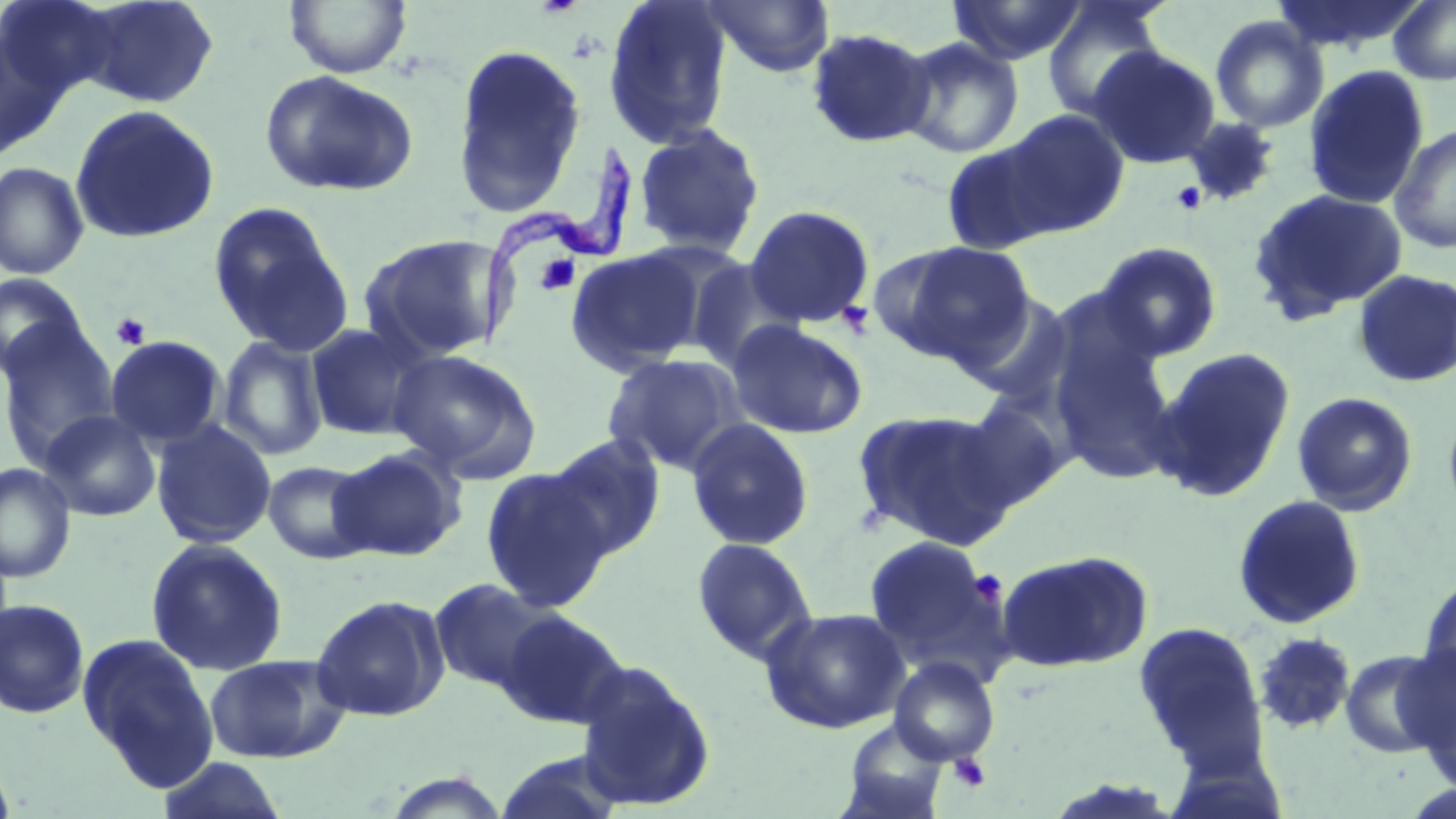
Summary:
  - Coordinate format: approximate bounding boxes as (x1, y1, x2, y2) in pixels
  - Platelet locations: (1172, 182, 1206, 214), (535, 254, 581, 296), (844, 301, 878, 333), (110, 313, 151, 349), (967, 569, 1008, 606), (947, 753, 991, 793)
  - Uninfected red blood cell locations: (1, 0, 115, 107), (75, 0, 220, 108), (284, 0, 411, 78), (602, 0, 734, 150), (701, 0, 835, 78), (947, 0, 1088, 66), (1388, 0, 1456, 86), (1041, 1, 1169, 122), (1210, 15, 1328, 132), (805, 27, 936, 149), (0, 31, 61, 161), (897, 37, 1025, 159), (450, 42, 588, 217), (1088, 45, 1221, 168), (1303, 64, 1430, 210), (259, 69, 418, 198), (68, 104, 220, 244), (999, 108, 1130, 238), (1182, 116, 1281, 206), (1390, 122, 1456, 254), (632, 123, 766, 258), (941, 138, 1061, 255), (0, 161, 90, 280), (1247, 187, 1408, 324), (207, 202, 353, 357), (745, 205, 875, 328), (359, 234, 507, 363), (874, 240, 1036, 366), (1094, 241, 1223, 361), (566, 247, 706, 374), (686, 259, 803, 373), (1352, 269, 1456, 389), (0, 274, 88, 380), (953, 288, 1077, 411), (0, 320, 121, 468), (726, 320, 868, 440), (304, 323, 429, 442), (1048, 327, 1185, 485), (105, 335, 226, 448), (217, 335, 328, 462), (1151, 348, 1296, 502), (387, 350, 542, 479), (601, 354, 747, 476), (1291, 391, 1419, 516), (952, 398, 1071, 511), (853, 408, 1017, 549), (41, 410, 161, 522), (685, 419, 814, 551), (151, 420, 277, 549), (545, 432, 668, 561), (329, 447, 465, 561), (263, 460, 375, 563), (0, 462, 75, 582), (480, 467, 615, 613), (1231, 494, 1367, 630), (862, 534, 1006, 673), (691, 537, 817, 664), (145, 538, 288, 676), (996, 549, 1153, 673), (1418, 570, 1456, 693), (428, 577, 557, 693), (311, 593, 449, 722), (0, 598, 90, 718), (760, 606, 911, 734), (498, 609, 629, 729), (1132, 620, 1268, 769), (1252, 632, 1357, 734), (78, 633, 219, 790), (1339, 647, 1448, 759), (1407, 650, 1456, 789), (203, 653, 350, 763), (888, 657, 1001, 766), (574, 660, 717, 812), (840, 718, 950, 818), (0, 748, 17, 819), (157, 755, 288, 818), (380, 770, 511, 818)
  - Trypanosoma brucei locations: (477, 136, 640, 356)
  - Slide-level diagnosis: Trypanosoma brucei
  - Modality: light microscopy
  - Image size: 1456×819 pixels
  - Magnification: 1000x
  - Field of view: one of a larger specimen
  - Preparation: thin blood film
  - Stain: May-Grünwald-Giemsa